State which parasite is depicted.
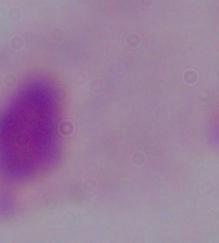

This is a trichomonad.

modality: micrograph
magnification: 1000x